Classify this cell by malaria status.
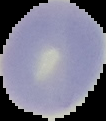

Uninfected.

Summary:
  - Preparation: thin blood film
  - Image size: 106×121 pixels
  - Image type: cell region segmented out of the field of view; surrounding area masked to black